Identify the blood parasite species.
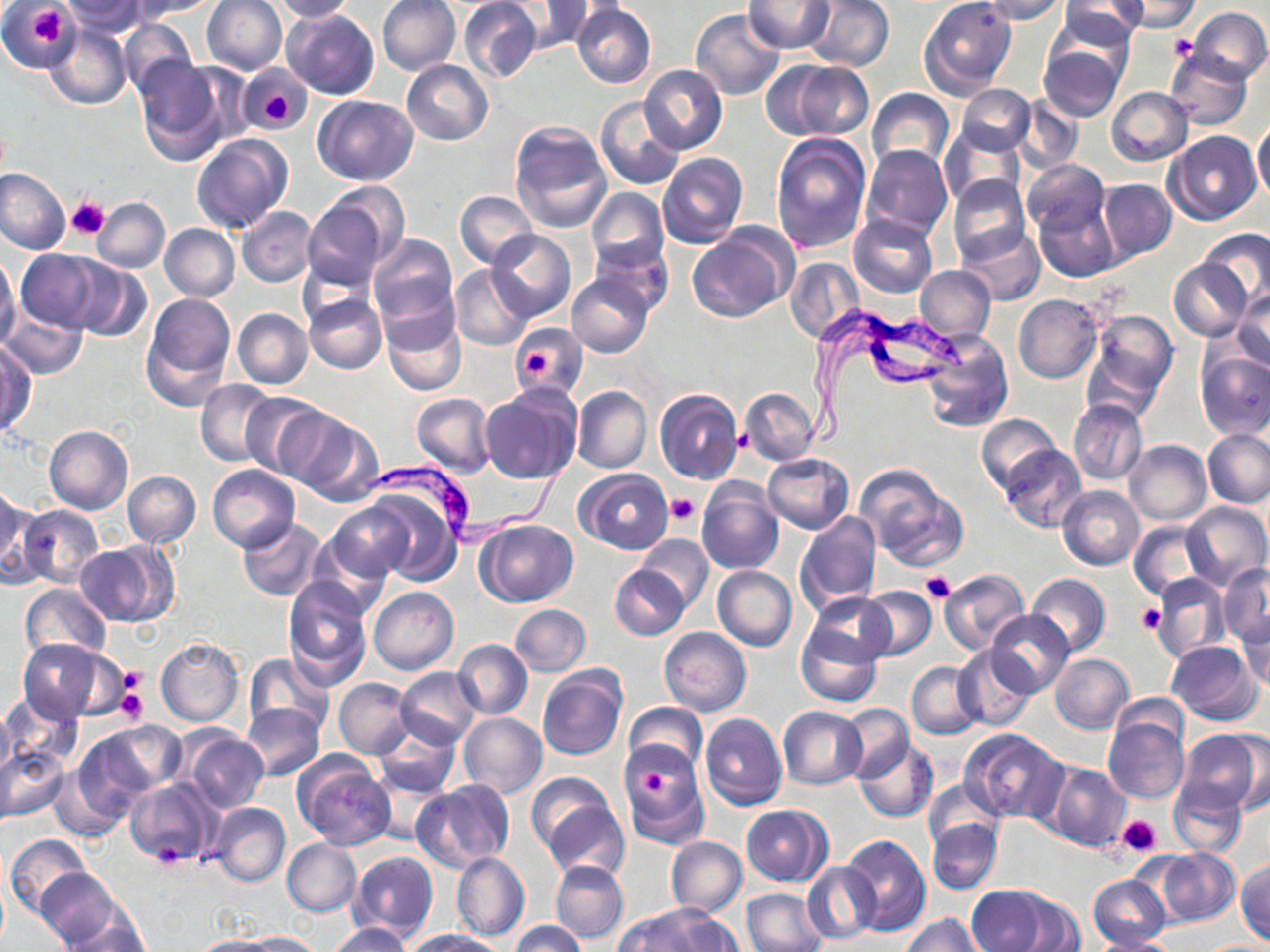

Trypanosoma brucei.

image size = 1270×952 pixels
field of view = single
stain = May-Grünwald-Giemsa
modality = light microscopy
Trypanosoma brucei locations = approximate bounding boxes as (x1,y1)-(x2,y2) corner pairs in pixels: (804,307)-(967,455), (362,452)-(576,549)
platelet locations = approximate bounding boxes as (x1,y1)-(x2,y2) corner pairs in pixels: (29,8)-(65,46), (1167,35)-(1199,62), (261,93)-(296,124), (65,197)-(110,241), (525,350)-(553,379), (665,493)-(701,528), (921,573)-(955,604), (1136,603)-(1166,634), (119,666)-(146,697), (116,688)-(147,725), (645,767)-(669,801), (1118,816)-(1161,856), (151,841)-(189,871)
preparation = thin blood smear
uninfected red blood cell locations = approximate bounding boxes as (x1,y1)-(x2,y2) corner pairs in pixels: (55,0)-(148,35), (131,0)-(222,19), (201,0)-(288,75), (270,0)-(355,21), (376,0)-(461,77), (459,0)-(544,83), (802,0)-(894,71), (919,0)-(1017,99), (979,0)-(1065,23), (1115,0)-(1199,32), (743,1)-(836,54), (1057,1)-(1146,48), (2,2)-(77,74), (504,2)-(589,54), (571,4)-(656,89), (1047,5)-(1139,88), (280,7)-(378,101), (1187,7)-(1270,84), (691,8)-(786,100), (120,20)-(199,96), (44,24)-(133,109), (1038,44)-(1126,121), (1165,48)-(1254,130), (134,58)-(234,163), (774,59)-(874,141), (402,60)-(494,145), (239,64)-(310,133), (639,65)-(727,154), (957,84)-(1035,156), (1107,87)-(1193,165), (866,88)-(955,173), (313,94)-(419,184), (1013,94)-(1083,173), (596,96)-(685,190), (1251,121)-(1270,201), (509,122)-(612,232), (940,127)-(1025,209), (1166,131)-(1261,225), (770,133)-(872,255), (192,134)-(292,234), (862,145)-(952,241), (656,153)-(748,248), (1023,159)-(1110,235), (0,168)-(71,254), (948,175)-(1030,266), (1097,179)-(1177,264), (586,187)-(670,273), (455,190)-(538,269), (300,194)-(399,289), (93,198)-(170,272), (1032,198)-(1121,281), (237,207)-(317,287), (847,214)-(937,299), (159,224)-(240,301), (959,226)-(1045,305), (685,229)-(792,324), (1200,229)-(1270,307), (486,230)-(577,322), (369,234)-(459,329), (588,243)-(671,315), (16,250)-(103,331), (0,256)-(22,349), (1169,257)-(1253,342), (786,258)-(864,342), (70,261)-(152,343), (450,265)-(535,351), (914,265)-(996,343), (566,272)-(654,358), (1231,287)-(1270,371), (138,293)-(234,408), (304,294)-(387,374), (1014,294)-(1102,384), (1,305)-(87,378), (233,308)-(313,389), (1084,309)-(1178,413), (382,311)-(466,395), (510,328)-(587,397), (920,329)-(1013,432), (1,344)-(36,436), (1195,350)-(1270,439), (196,378)-(278,467), (572,385)-(652,474), (481,387)-(581,486), (654,388)-(744,485), (740,388)-(818,466), (242,393)-(328,478), (410,393)-(496,477), (1067,399)-(1147,485), (274,408)-(373,501), (977,413)-(1063,497), (44,426)-(133,515), (1203,430)-(1270,509), (1123,439)-(1211,524), (998,446)-(1086,531), (762,453)-(854,533), (853,463)-(965,570), (207,466)-(300,552), (576,468)-(674,554), (123,471)-(201,548), (696,477)-(784,574), (361,483)-(466,583), (1057,485)-(1145,570), (1,489)-(36,585), (1181,501)-(1270,591), (327,502)-(415,581), (19,505)-(103,588), (794,509)-(881,613), (237,519)-(324,600), (474,519)-(578,608), (1126,521)-(1209,600), (635,534)-(715,612), (74,541)-(177,627), (611,564)-(687,640), (1218,565)-(1270,648), (713,566)-(796,651), (938,568)-(1030,656), (1026,573)-(1110,657), (1151,573)-(1230,663), (284,578)-(373,689), (20,583)-(112,663), (858,585)-(937,661), (369,587)-(459,675), (806,593)-(893,668), (510,604)-(590,676), (985,611)-(1073,697), (1234,612)-(1269,692), (795,622)-(883,707), (659,626)-(751,716), (19,637)-(117,724), (156,637)-(243,726), (453,639)-(533,719), (1166,640)-(1262,724), (953,646)-(1037,732), (245,653)-(336,739), (1048,653)-(1133,734), (906,662)-(982,739), (537,666)-(626,760), (396,667)-(483,750), (334,678)-(416,759), (2,690)-(81,769), (0,700)-(14,783), (241,702)-(325,780), (623,703)-(707,774), (840,704)-(914,783), (778,706)-(868,789), (458,712)-(547,800), (700,712)-(787,809), (1103,715)-(1187,804), (91,720)-(186,799), (373,724)-(460,797), (176,728)-(270,814), (958,728)-(1067,822), (1178,729)-(1268,818), (853,739)-(939,822), (618,742)-(710,848), (1,746)-(70,821), (291,754)-(396,850), (1038,760)-(1132,852), (48,764)-(127,842), (524,771)-(614,855), (924,779)-(1003,849), (124,780)-(217,868), (412,780)-(514,871), (1169,783)-(1248,857), (533,792)-(630,883), (208,803)-(290,886), (740,805)-(833,886), (926,819)-(1002,895), (6,834)-(95,918), (840,835)-(932,936), (667,836)-(746,918), (282,839)-(362,915), (1151,848)-(1241,926), (348,851)-(437,942), (449,851)-(529,941), (1235,859)-(1270,944), (551,860)-(629,944), (803,861)-(878,944), (36,868)-(121,948), (1089,875)-(1171,948), (0,880)-(9,952), (965,885)-(1078,952), (740,888)-(826,952), (623,906)-(735,952), (57,909)-(151,952), (903,915)-(984,952), (509,920)-(586,952), (327,922)-(414,952), (404,929)-(505,952), (238,931)-(325,951), (1086,935)-(1179,952), (190,936)-(285,952), (1201,941)-(1268,951)
magnification = 1000x